Give the preparation type.
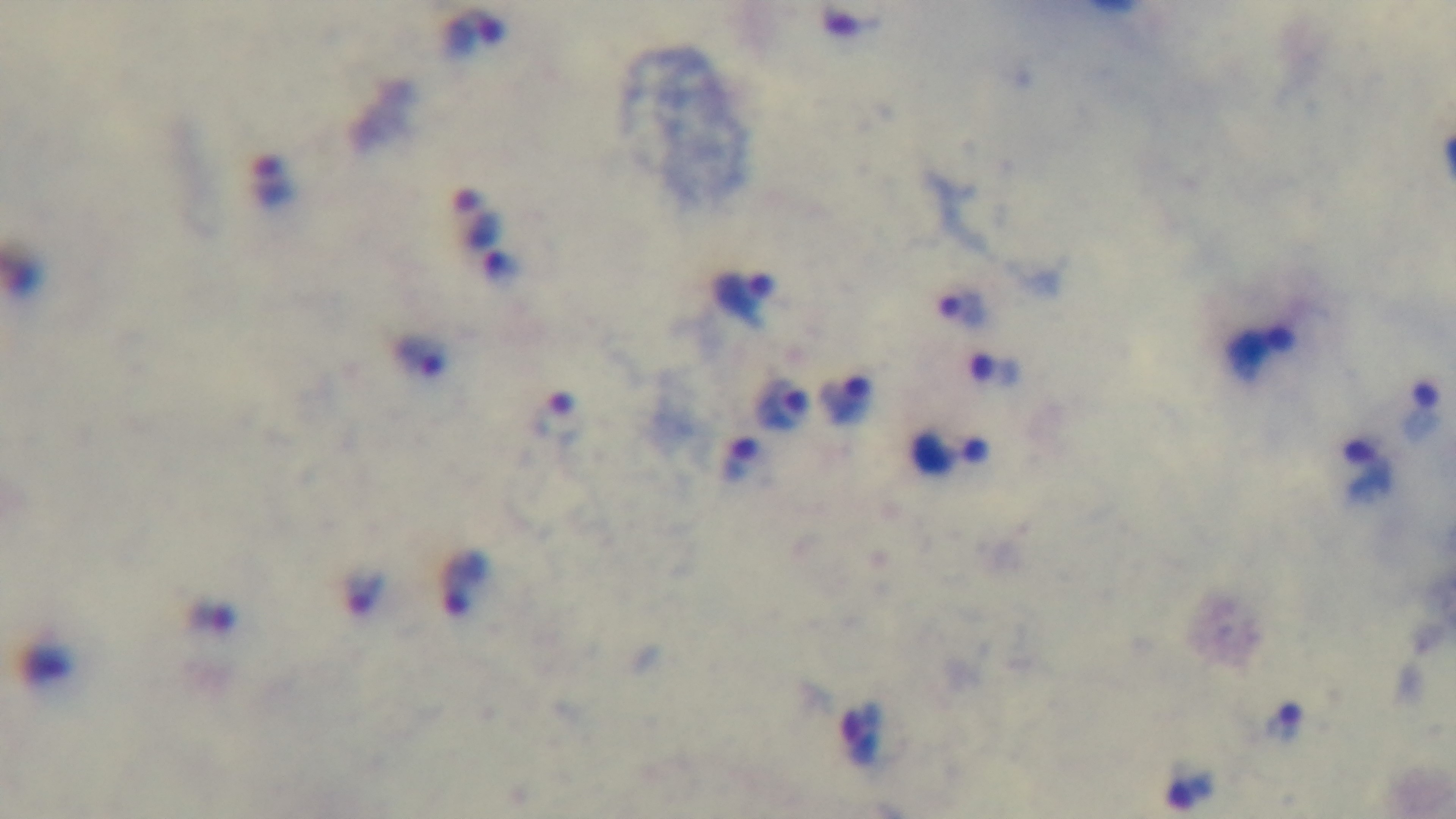
It is a thick blood film.

Summary:
  - Modality: light microscopy
  - Malaria status: positive
  - Field of view: one from the slide
  - Capture: mounted 4K digital camera
  - Stain: Giemsa
  - Objective: 100x oil immersion